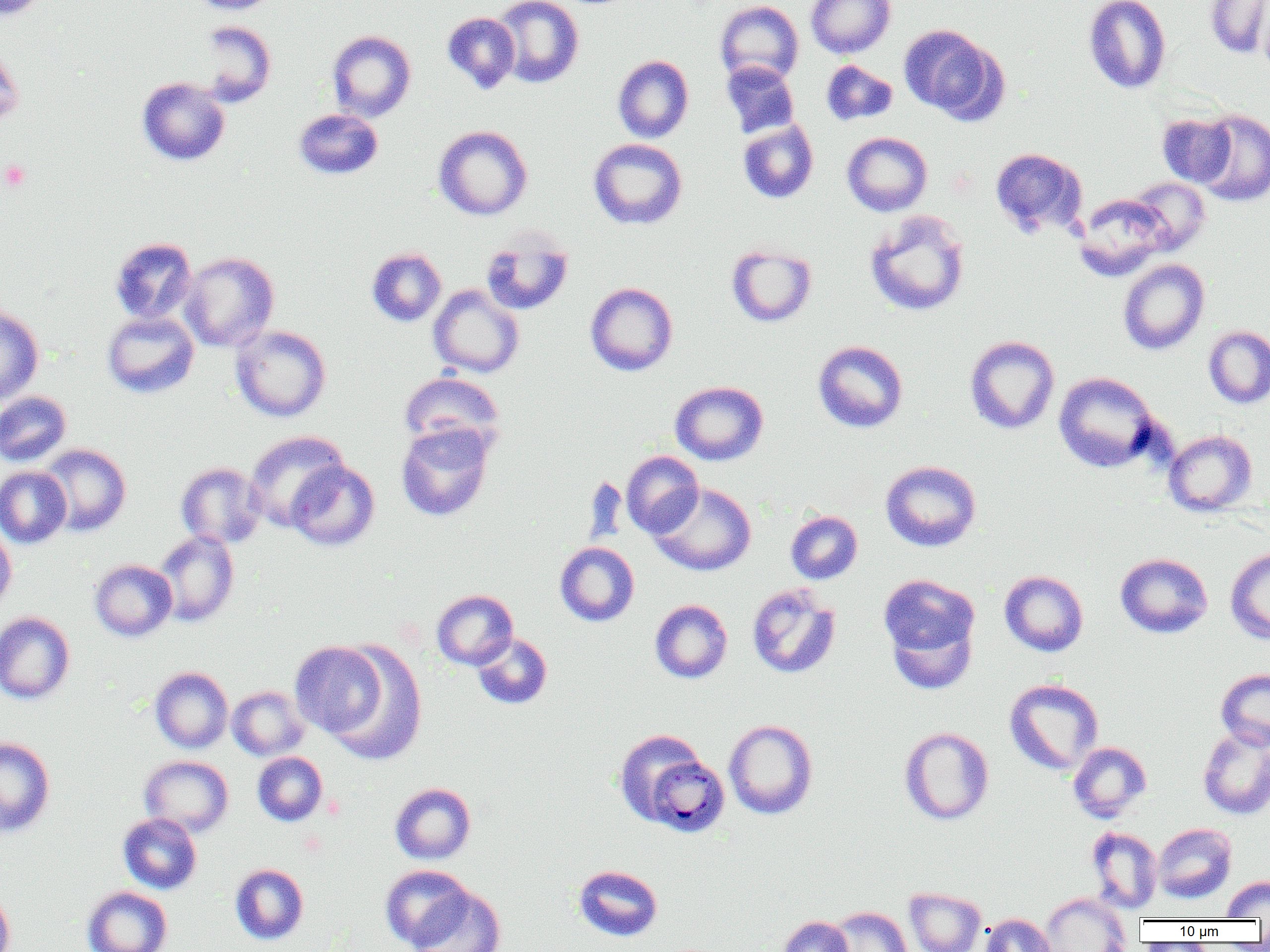 Approximate bounding boxes as named x1/y1/x2/y2 corners in pixels. Plasmodium malariae-infected red blood cell locations: (x1=643, y1=755, x2=730, y2=837). Platelet locations: (x1=1, y1=159, x2=31, y2=192). Uninfected red blood cell locations: (x1=1, y1=0, x2=50, y2=21), (x1=188, y1=0, x2=280, y2=14), (x1=493, y1=0, x2=584, y2=88), (x1=805, y1=0, x2=896, y2=58), (x1=1083, y1=0, x2=1172, y2=94), (x1=1204, y1=0, x2=1270, y2=58), (x1=714, y1=1, x2=804, y2=87), (x1=1257, y1=2, x2=1270, y2=78), (x1=441, y1=12, x2=521, y2=94), (x1=198, y1=20, x2=277, y2=106), (x1=899, y1=24, x2=1003, y2=122), (x1=327, y1=30, x2=416, y2=122), (x1=0, y1=39, x2=25, y2=128), (x1=613, y1=55, x2=694, y2=143), (x1=821, y1=60, x2=898, y2=126), (x1=721, y1=61, x2=800, y2=139), (x1=137, y1=77, x2=230, y2=166), (x1=294, y1=109, x2=383, y2=180), (x1=1192, y1=109, x2=1270, y2=207), (x1=1156, y1=113, x2=1236, y2=187), (x1=738, y1=119, x2=819, y2=203), (x1=433, y1=125, x2=532, y2=221), (x1=842, y1=132, x2=932, y2=216), (x1=588, y1=138, x2=688, y2=230), (x1=989, y1=147, x2=1088, y2=238), (x1=1126, y1=177, x2=1210, y2=255), (x1=1074, y1=193, x2=1171, y2=280), (x1=864, y1=210, x2=970, y2=317), (x1=480, y1=229, x2=574, y2=316), (x1=109, y1=237, x2=197, y2=325), (x1=726, y1=243, x2=817, y2=327), (x1=366, y1=247, x2=447, y2=326), (x1=180, y1=252, x2=279, y2=352), (x1=1118, y1=259, x2=1210, y2=355), (x1=585, y1=282, x2=678, y2=376), (x1=427, y1=284, x2=524, y2=378), (x1=0, y1=304, x2=44, y2=406), (x1=102, y1=311, x2=199, y2=399), (x1=230, y1=325, x2=332, y2=422), (x1=1203, y1=326, x2=1270, y2=409), (x1=964, y1=335, x2=1060, y2=435), (x1=813, y1=340, x2=909, y2=433), (x1=399, y1=371, x2=505, y2=457), (x1=1053, y1=372, x2=1159, y2=473), (x1=670, y1=380, x2=769, y2=465), (x1=0, y1=391, x2=72, y2=467), (x1=396, y1=421, x2=495, y2=522), (x1=1163, y1=430, x2=1257, y2=516), (x1=244, y1=431, x2=349, y2=530), (x1=37, y1=443, x2=131, y2=536), (x1=621, y1=451, x2=703, y2=538), (x1=285, y1=460, x2=380, y2=551), (x1=880, y1=460, x2=981, y2=552), (x1=176, y1=462, x2=267, y2=549), (x1=0, y1=466, x2=72, y2=548), (x1=650, y1=482, x2=757, y2=576), (x1=785, y1=510, x2=863, y2=585), (x1=0, y1=525, x2=16, y2=615), (x1=153, y1=531, x2=239, y2=627), (x1=554, y1=542, x2=639, y2=627), (x1=1225, y1=547, x2=1270, y2=644), (x1=1114, y1=553, x2=1213, y2=638), (x1=89, y1=559, x2=177, y2=641), (x1=999, y1=570, x2=1088, y2=657), (x1=878, y1=573, x2=981, y2=679), (x1=746, y1=582, x2=841, y2=679), (x1=431, y1=589, x2=517, y2=670), (x1=649, y1=599, x2=733, y2=684), (x1=0, y1=612, x2=75, y2=704), (x1=471, y1=633, x2=552, y2=709), (x1=290, y1=640, x2=391, y2=742), (x1=324, y1=642, x2=428, y2=764), (x1=150, y1=666, x2=233, y2=753), (x1=1216, y1=668, x2=1270, y2=750), (x1=1004, y1=678, x2=1104, y2=774), (x1=227, y1=685, x2=310, y2=760), (x1=723, y1=719, x2=818, y2=819), (x1=899, y1=726, x2=994, y2=825), (x1=1198, y1=727, x2=1270, y2=820), (x1=614, y1=729, x2=711, y2=827), (x1=0, y1=737, x2=55, y2=837), (x1=1067, y1=741, x2=1152, y2=823), (x1=252, y1=751, x2=328, y2=826), (x1=139, y1=755, x2=233, y2=837), (x1=390, y1=782, x2=476, y2=864), (x1=118, y1=813, x2=202, y2=894), (x1=1152, y1=823, x2=1237, y2=903), (x1=1086, y1=826, x2=1163, y2=914), (x1=230, y1=863, x2=309, y2=944), (x1=572, y1=864, x2=663, y2=941), (x1=380, y1=865, x2=472, y2=949), (x1=1221, y1=876, x2=1270, y2=919), (x1=407, y1=885, x2=506, y2=952), (x1=82, y1=886, x2=172, y2=952), (x1=904, y1=887, x2=986, y2=952), (x1=0, y1=888, x2=15, y2=952), (x1=1040, y1=893, x2=1131, y2=952), (x1=827, y1=906, x2=913, y2=952), (x1=980, y1=913, x2=1055, y2=952), (x1=778, y1=915, x2=853, y2=952). Slide-level diagnosis: Plasmodium malariae. Image is 1270×952 pixels. Captured at 1000x magnification. Single field of view. Thin blood smear. Optical microscopy.